Locate every Trypanosoma brucei.
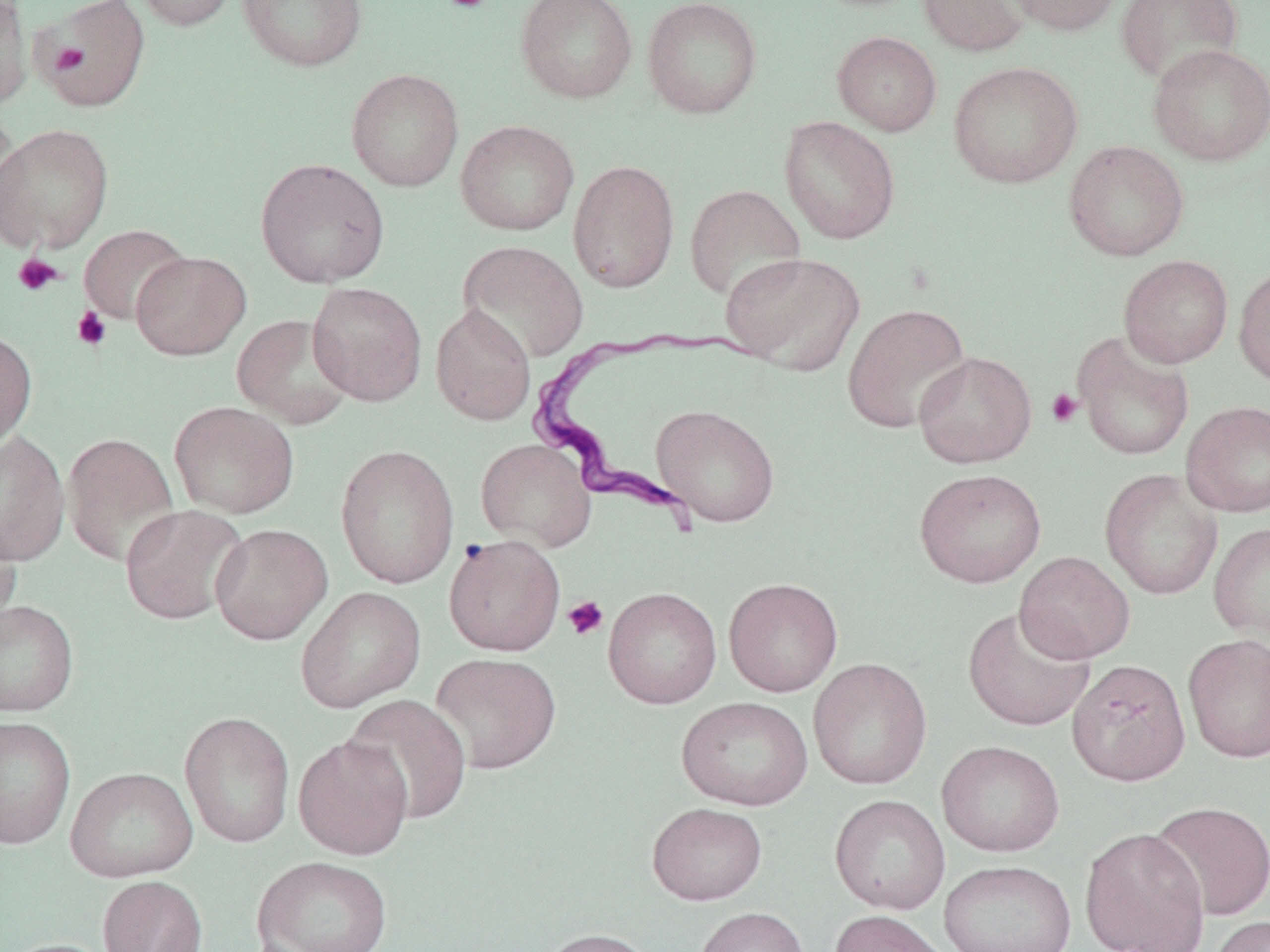
Approximate bounding boxes as named x1/y1/x2/y2 corners in pixels.
Trypanosoma brucei: (x1=525, y1=325, x2=768, y2=524).

Summary:
  - Uninfected red blood cell locations: (x1=0, y1=0, x2=33, y2=110), (x1=130, y1=0, x2=241, y2=32), (x1=238, y1=0, x2=368, y2=72), (x1=515, y1=0, x2=638, y2=103), (x1=642, y1=0, x2=763, y2=118), (x1=918, y1=0, x2=1032, y2=56), (x1=1004, y1=0, x2=1125, y2=36), (x1=1115, y1=0, x2=1243, y2=85), (x1=37, y1=1, x2=150, y2=112), (x1=832, y1=31, x2=942, y2=136), (x1=1148, y1=44, x2=1270, y2=167), (x1=948, y1=61, x2=1083, y2=189), (x1=346, y1=68, x2=464, y2=192), (x1=0, y1=106, x2=24, y2=242), (x1=779, y1=116, x2=900, y2=244), (x1=456, y1=120, x2=579, y2=235), (x1=0, y1=122, x2=114, y2=254), (x1=1063, y1=140, x2=1189, y2=261), (x1=255, y1=157, x2=390, y2=288), (x1=568, y1=159, x2=680, y2=293), (x1=685, y1=184, x2=806, y2=302), (x1=79, y1=224, x2=191, y2=325), (x1=457, y1=240, x2=589, y2=363), (x1=130, y1=251, x2=251, y2=360), (x1=720, y1=251, x2=865, y2=375), (x1=1118, y1=255, x2=1233, y2=368), (x1=1233, y1=263, x2=1270, y2=389), (x1=307, y1=282, x2=427, y2=406), (x1=842, y1=303, x2=971, y2=433), (x1=430, y1=304, x2=536, y2=426), (x1=232, y1=313, x2=355, y2=429), (x1=0, y1=328, x2=37, y2=448), (x1=1072, y1=332, x2=1194, y2=461), (x1=913, y1=351, x2=1037, y2=467), (x1=1181, y1=400, x2=1270, y2=518), (x1=169, y1=401, x2=299, y2=519), (x1=652, y1=404, x2=780, y2=527), (x1=0, y1=430, x2=70, y2=567), (x1=61, y1=433, x2=180, y2=568), (x1=476, y1=438, x2=597, y2=552), (x1=336, y1=443, x2=459, y2=589), (x1=914, y1=468, x2=1046, y2=588), (x1=1099, y1=468, x2=1223, y2=601), (x1=119, y1=504, x2=249, y2=625), (x1=0, y1=521, x2=21, y2=635), (x1=1208, y1=522, x2=1270, y2=642), (x1=210, y1=523, x2=332, y2=645), (x1=444, y1=534, x2=565, y2=656), (x1=1014, y1=552, x2=1135, y2=663), (x1=723, y1=577, x2=843, y2=697), (x1=295, y1=585, x2=426, y2=714), (x1=603, y1=587, x2=722, y2=709), (x1=0, y1=599, x2=79, y2=716), (x1=963, y1=606, x2=1094, y2=732), (x1=1183, y1=634, x2=1270, y2=764), (x1=429, y1=652, x2=561, y2=774), (x1=808, y1=658, x2=932, y2=789), (x1=1067, y1=658, x2=1191, y2=786), (x1=343, y1=694, x2=473, y2=825), (x1=676, y1=696, x2=813, y2=810), (x1=179, y1=711, x2=295, y2=848), (x1=0, y1=715, x2=76, y2=849), (x1=293, y1=735, x2=414, y2=860), (x1=936, y1=740, x2=1064, y2=857), (x1=65, y1=766, x2=198, y2=882), (x1=829, y1=794, x2=950, y2=914), (x1=1148, y1=801, x2=1270, y2=921), (x1=647, y1=802, x2=767, y2=905), (x1=1079, y1=826, x2=1211, y2=952), (x1=252, y1=856, x2=393, y2=951), (x1=938, y1=859, x2=1077, y2=952), (x1=98, y1=875, x2=207, y2=952), (x1=694, y1=906, x2=809, y2=952), (x1=828, y1=909, x2=954, y2=952), (x1=1207, y1=915, x2=1270, y2=952), (x1=536, y1=927, x2=659, y2=952), (x1=0, y1=938, x2=119, y2=952)
  - Platelet locations: (x1=442, y1=0, x2=493, y2=13), (x1=49, y1=44, x2=88, y2=74), (x1=13, y1=253, x2=64, y2=297), (x1=72, y1=307, x2=112, y2=351), (x1=1046, y1=388, x2=1083, y2=428), (x1=562, y1=596, x2=609, y2=640)
  - Slide-level diagnosis: Trypanosoma brucei
  - Image size: 1270×952 pixels
  - Preparation: thin blood smear
  - Modality: optical microscopy
  - Stain: May-Grünwald-Giemsa
  - Field of view: one of a larger specimen
  - Magnification: 1000x